Identify the parasite.
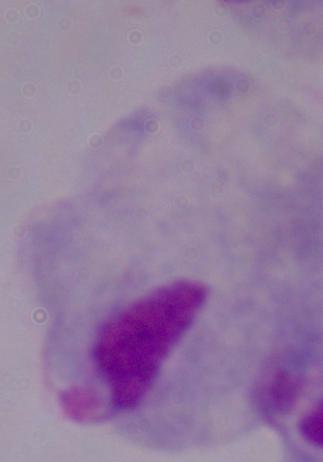
This is a trichomonad.

Micrograph. 1000x magnification.